Classify this cell by malaria status.
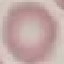

It is uninfected.

{
  "capture": "smartphone camera at the microscope eyepiece",
  "stain": "Giemsa",
  "preparation": "thin smear",
  "image_type": "cell patch, automatically extracted from a larger field of view and resized to 64 × 64 pixels"
}